Report the malaria status of this cell.
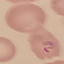

It is parasitized.

image type = cell patch, automatically extracted from a larger field of view and resized to 64 × 64 pixels
preparation = thin blood film
stain = Giemsa
capture = smartphone camera at the microscope eyepiece